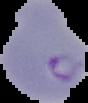
Segmented cell region on a black background. From a thin blood film. Malaria status: parasitized. Image is 88×103 pixels.